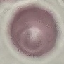
Summary:
  - Result: negative for malaria parasites
  - Preparation: thin blood smear
  - Capture: smartphone camera at the microscope eyepiece
  - Stain: Giemsa
  - Image type: cell patch, automatically extracted from a larger field of view and resized to 64 × 64 pixels